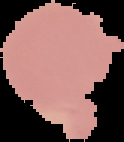

preparation = thin blood smear
image size = 124×142 pixels
image type = segmented cell region with the area outside set to black
malaria status = uninfected